Point out each malaria parasite.
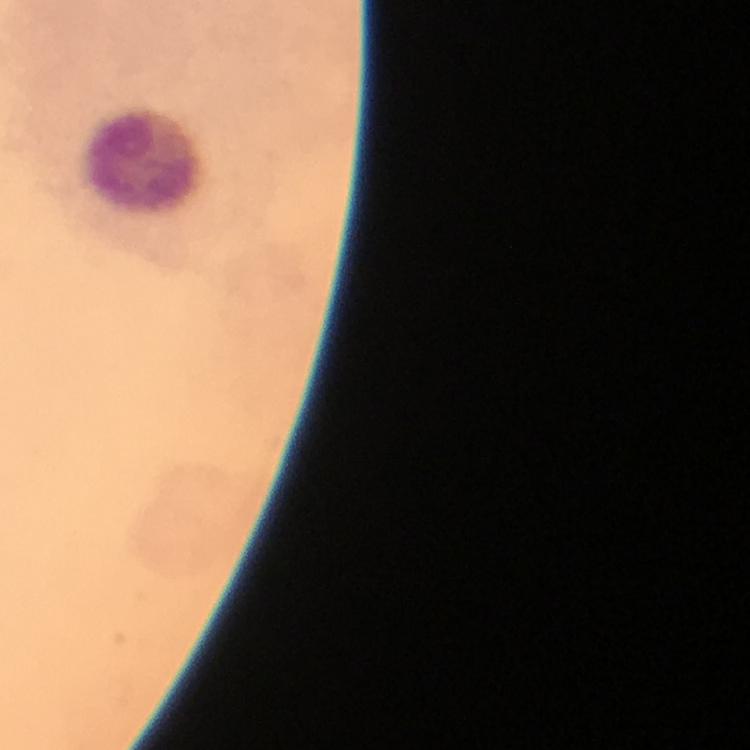
No malaria parasites detected.

Approximate object centers, in pixels from the top-left corner.
Summary:
  - Leukocyte locations: (x=143, y=164)
  - Immersion oil: applied
  - Preparation: thick blood smear
  - Stain: Giemsa
  - Context: from a malaria diagnostic workup
  - Cropped from: a single field of view
  - Magnification: 100x
  - Capture: smartphone camera through the microscope
  - Image size: 750×750 pixels